Name the blood parasite species.
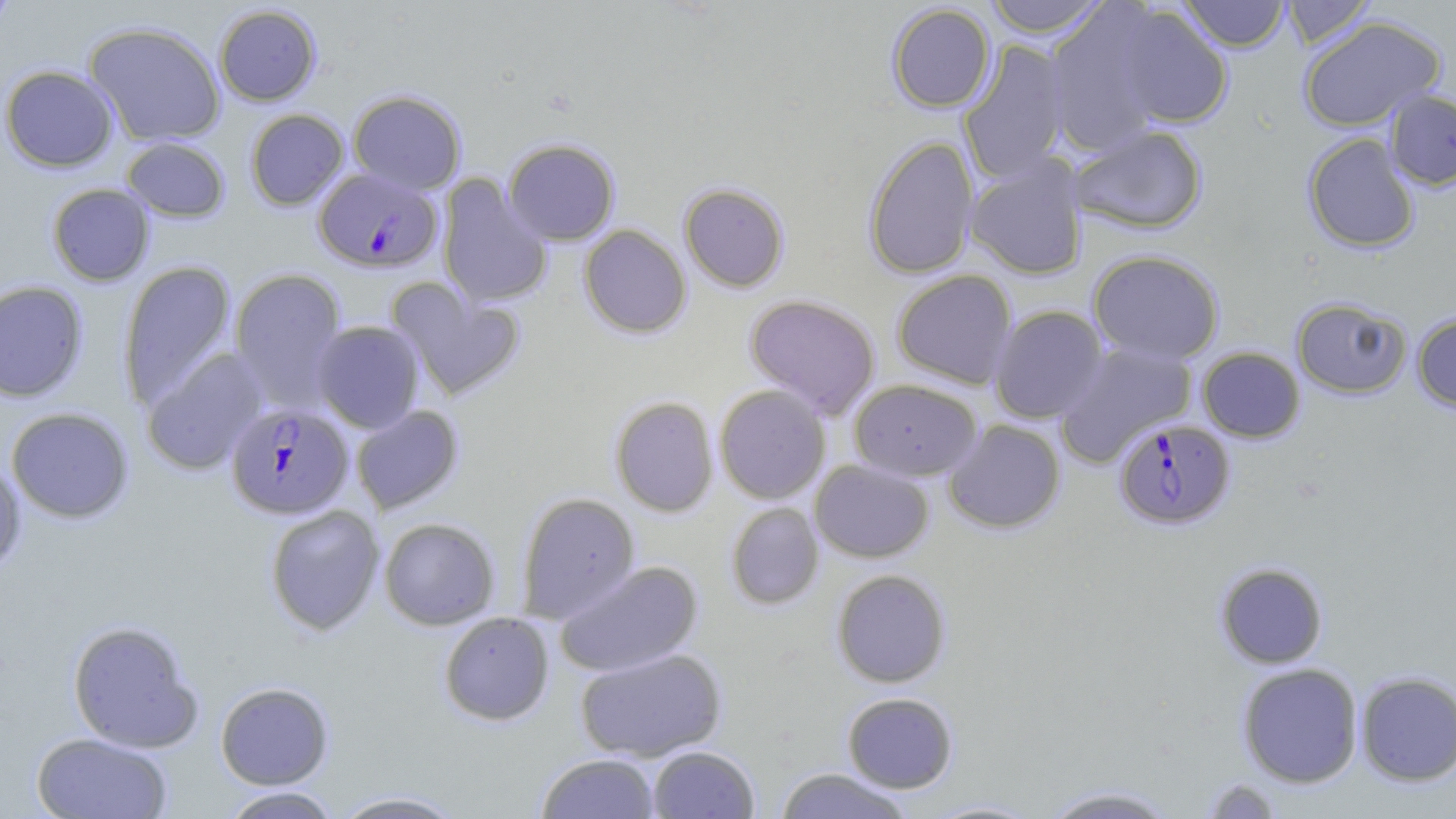
Plasmodium falciparum.

field of view = single
modality = light microscopy
uninfected red blood cell locations = approximate bounding boxes as (x1,y1)-(x2,y2) corner pairs in pixels: (0,0)-(21,30), (983,0)-(1110,38), (1177,0)-(1290,51), (1280,1)-(1377,48), (886,3)-(996,112), (213,5)-(322,106), (1108,5)-(1234,130), (1045,6)-(1170,154), (1298,16)-(1446,131), (84,21)-(226,147), (958,40)-(1072,184), (0,65)-(118,172), (348,90)-(466,195), (1385,90)-(1456,191), (244,109)-(349,210), (1068,124)-(1209,234), (1302,132)-(1420,253), (862,136)-(980,279), (121,137)-(231,222), (503,138)-(620,246), (965,154)-(1089,280), (437,174)-(553,309), (678,182)-(790,292), (46,183)-(155,286), (579,224)-(691,338), (1088,249)-(1225,364), (118,261)-(237,409), (229,267)-(348,407), (891,269)-(1017,389), (386,280)-(525,401), (0,281)-(89,402), (744,294)-(881,418), (1291,297)-(1411,398), (989,305)-(1108,423), (1411,312)-(1456,412), (312,321)-(424,433), (1054,340)-(1198,466), (1197,346)-(1305,442), (141,348)-(268,476), (848,379)-(982,481), (714,384)-(831,504), (609,396)-(719,517), (350,405)-(464,514), (6,407)-(134,523), (943,419)-(1066,534), (0,458)-(26,576), (810,460)-(933,563), (516,491)-(640,623), (725,502)-(824,610), (264,504)-(385,636), (379,517)-(500,630), (555,560)-(704,678), (1215,562)-(1328,669), (831,569)-(951,687), (438,611)-(555,725), (67,620)-(202,752), (574,647)-(728,762), (1237,662)-(1363,787), (1355,671)-(1456,786), (215,682)-(334,789), (842,692)-(958,793), (32,732)-(173,819), (647,745)-(760,818), (536,753)-(660,818), (774,767)-(914,818), (1197,778)-(1285,818), (1038,784)-(1181,818), (218,786)-(341,818), (329,791)-(468,818), (919,798)-(1047,818)
stain = May-Grünwald-Giemsa
preparation = thin blood smear
image size = 1456×819 pixels
Plasmodium falciparum-infected red blood cell locations = approximate bounding boxes as (x1,y1)-(x2,y2) corner pairs in pixels: (313,167)-(443,274), (225,402)-(354,520), (1115,419)-(1234,529)
magnification = 1000x